Name the parasite shown.
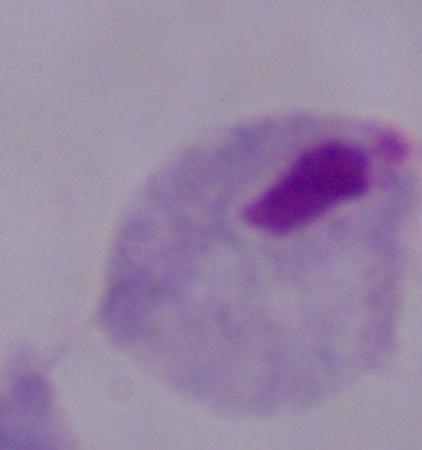

A trichomonad.

Summary:
  - Modality: micrograph
  - Magnification: 1000x